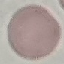

Summary:
  - Malaria status: uninfected
  - Capture: smartphone camera at the microscope eyepiece
  - Image type: cell patch, automatically extracted from a larger field of view and resized to 64 × 64 pixels
  - Stain: Giemsa
  - Preparation: thin blood film